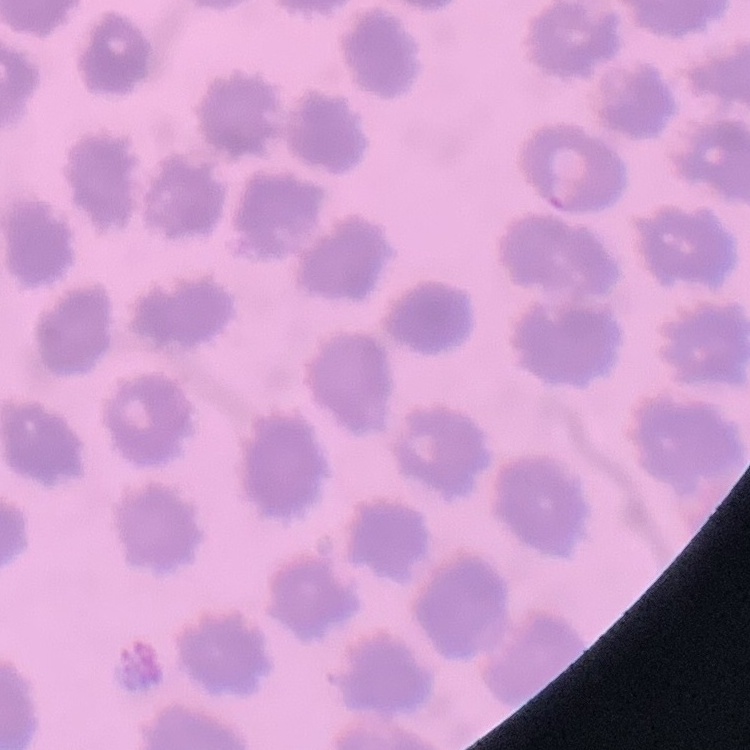
Summary:
  - Erythrocyte morphology: no rouleaux formation
  - Image type: square crop of a larger photomicrograph
  - Stain: Field's or Giemsa
  - Preparation: thin blood film